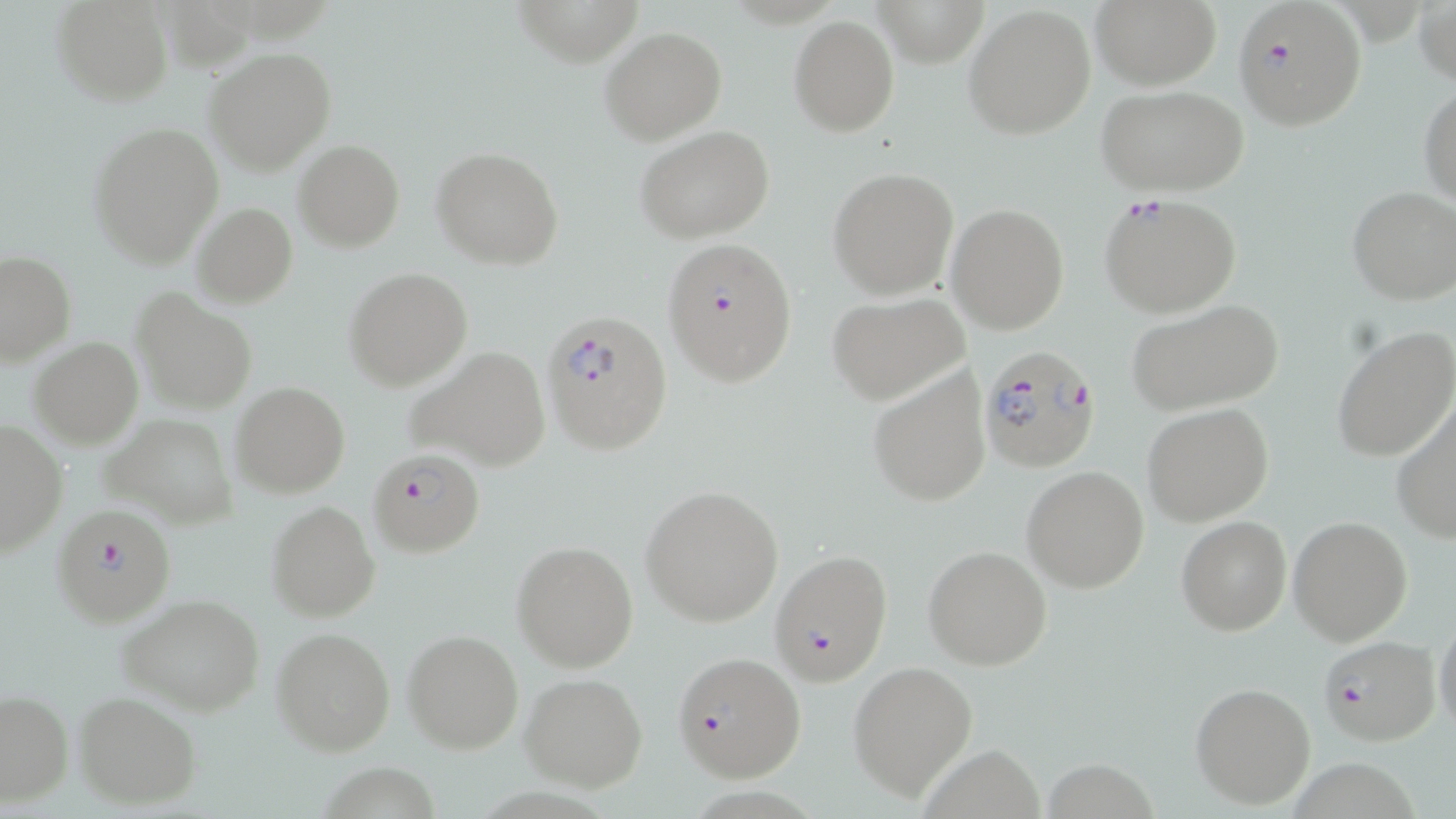

slide-level diagnosis = Plasmodium falciparum
modality = light microscopy
image size = 1456×819 pixels
stain = May-Grünwald-Giemsa
magnification = 1000x
preparation = thin blood film
Plasmodium falciparum-infected red blood cell locations = approximate bounding boxes as (x1, y1, x2, y2) in pixels: (1231, 0, 1368, 130), (1098, 193, 1244, 318), (662, 236, 799, 387), (540, 309, 671, 453), (976, 343, 1103, 471), (368, 446, 486, 558), (51, 504, 177, 629), (769, 550, 894, 686), (1317, 635, 1440, 748), (671, 652, 806, 782)
field of view = single
uninfected red blood cell locations = approximate bounding boxes as (x1, y1, x2, y2) in pixels: (51, 0, 173, 106), (1091, 0, 1220, 90), (1416, 1, 1455, 89), (511, 2, 646, 68), (962, 3, 1096, 139), (862, 4, 995, 72), (189, 5, 332, 55), (790, 16, 898, 136), (600, 27, 726, 146), (204, 46, 337, 175), (1419, 81, 1456, 208), (1100, 86, 1247, 198), (88, 122, 223, 269), (637, 128, 774, 244), (293, 140, 404, 251), (431, 145, 563, 271), (828, 167, 958, 300), (1346, 185, 1456, 306), (192, 202, 298, 308), (948, 203, 1069, 334), (0, 251, 75, 367), (344, 268, 471, 389), (132, 289, 257, 414), (827, 293, 968, 403), (1124, 299, 1284, 417), (1333, 326, 1456, 464), (28, 337, 142, 449), (403, 347, 551, 472), (867, 363, 993, 507), (230, 383, 349, 499), (1391, 395, 1456, 544), (1142, 403, 1274, 527), (104, 414, 238, 528), (0, 419, 67, 559), (1022, 467, 1149, 593), (640, 485, 784, 626), (265, 501, 380, 622), (1176, 517, 1290, 636), (1288, 517, 1413, 646), (513, 540, 638, 672), (922, 545, 1053, 670), (119, 595, 264, 716), (1433, 606, 1456, 743), (272, 627, 395, 755), (403, 630, 523, 753), (849, 661, 978, 801), (520, 674, 649, 791), (1190, 681, 1315, 811), (0, 690, 73, 806), (72, 691, 200, 811), (925, 747, 1051, 819), (1043, 757, 1157, 818), (314, 759, 441, 816)